Assess this cell for malaria.
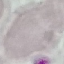

It is uninfected.

Summary:
  - Preparation: thin smear
  - Image type: cell patch, automatically extracted from a larger field of view and resized to 64 × 64 pixels
  - Stain: Giemsa
  - Capture: smartphone through the microscope eyepiece